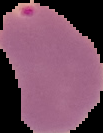

malaria status = parasitized
preparation = thin blood film
image size = 103×133 pixels
image type = cell region segmented out of the field of view; surrounding area masked to black